Assess the morphology of the red blood cells.
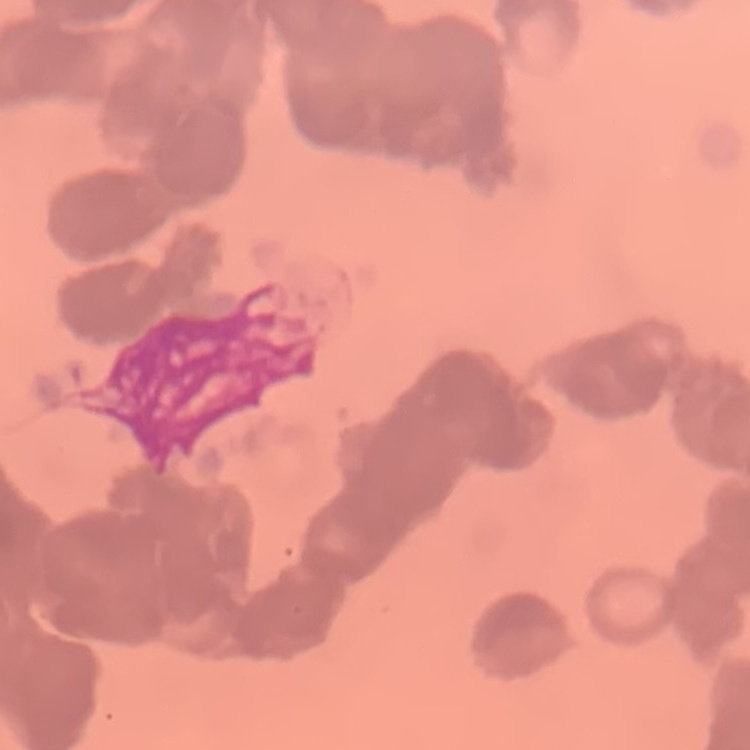

Rouleaux formation.

Thin peripheral smear. Field's or Giemsa stain. Square crop of a larger photomicrograph.